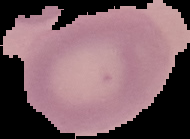

From a thin blood film. Malaria status: uninfected. Segmented cell region on a black background. Image is 190×139 pixels.